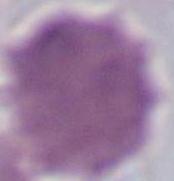
magnification = 1000x
modality = micrograph
identification = red blood cell